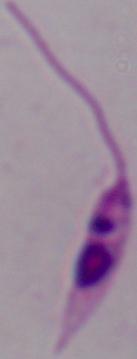
1000x magnification. Photomicrograph. A Leishmania parasite is seen.